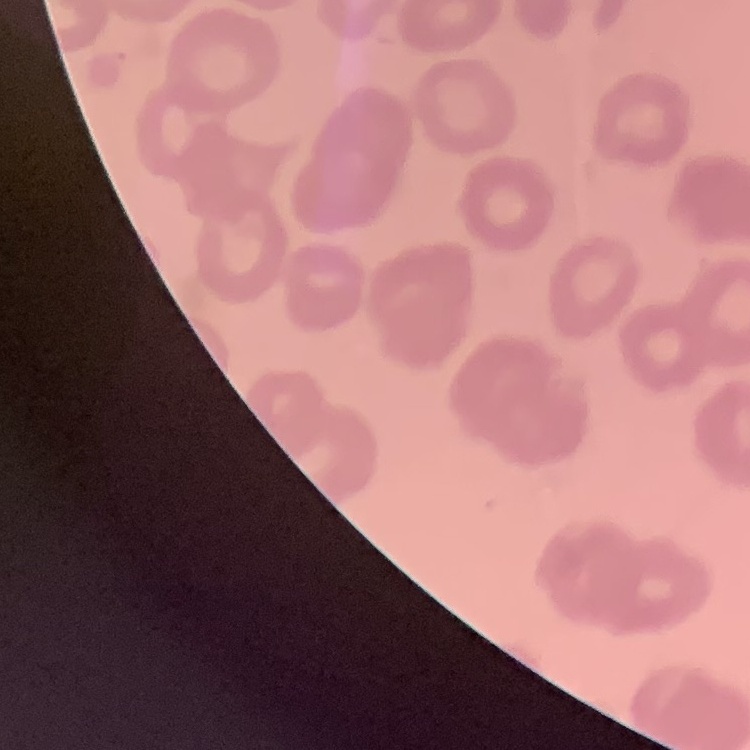

{
  "red_blood_cell_morphology": "no rouleaux formation",
  "image_type": "square crop of a larger photomicrograph",
  "preparation": "thin peripheral smear",
  "stain": "Field's or Giemsa"
}